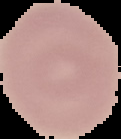
From a thin blood smear. Image is 121×139 pixels. Malaria status: uninfected. Cell region segmented out of the field of view; the surrounding area is masked to black.